Classify this cell by malaria status.
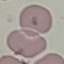

Uninfected.

Thin blood film. Cell patch, automatically extracted from a larger field of view and resized to 64 × 64 pixels. Giemsa-stained preparation. Acquired by smartphone through the microscope eyepiece.